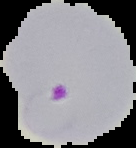

Summary:
  - Result: Plasmodium parasites identified
  - Image size: 136×148 pixels
  - Preparation: thin blood film
  - Image type: cell region segmented out of the field of view; surrounding area masked to black